Assess this cell for malaria.
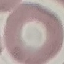

It is uninfected.

Giemsa stain. Photographed with a smartphone camera at the microscope eyepiece. Cell patch, automatically extracted from a larger field of view and resized to 64 × 64 pixels. Thin smear of blood.